Evaluate for malaria.
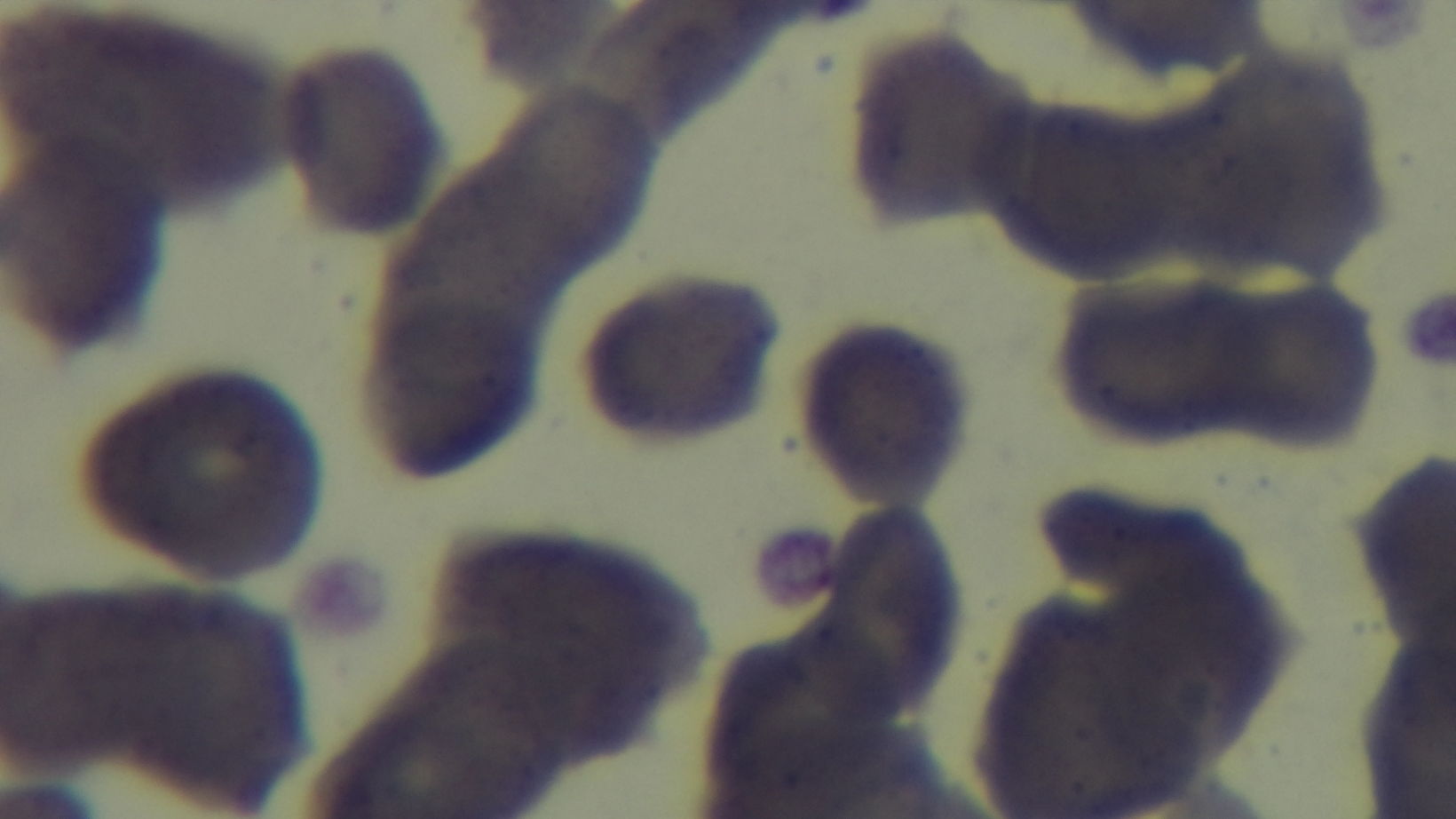

It is uninfected.

Summary:
  - Field of view: single
  - Objective: 100x oil immersion
  - Preparation: thin
  - Stain: Giemsa
  - Capture: mounted 4K digital camera
  - Modality: light microscopy